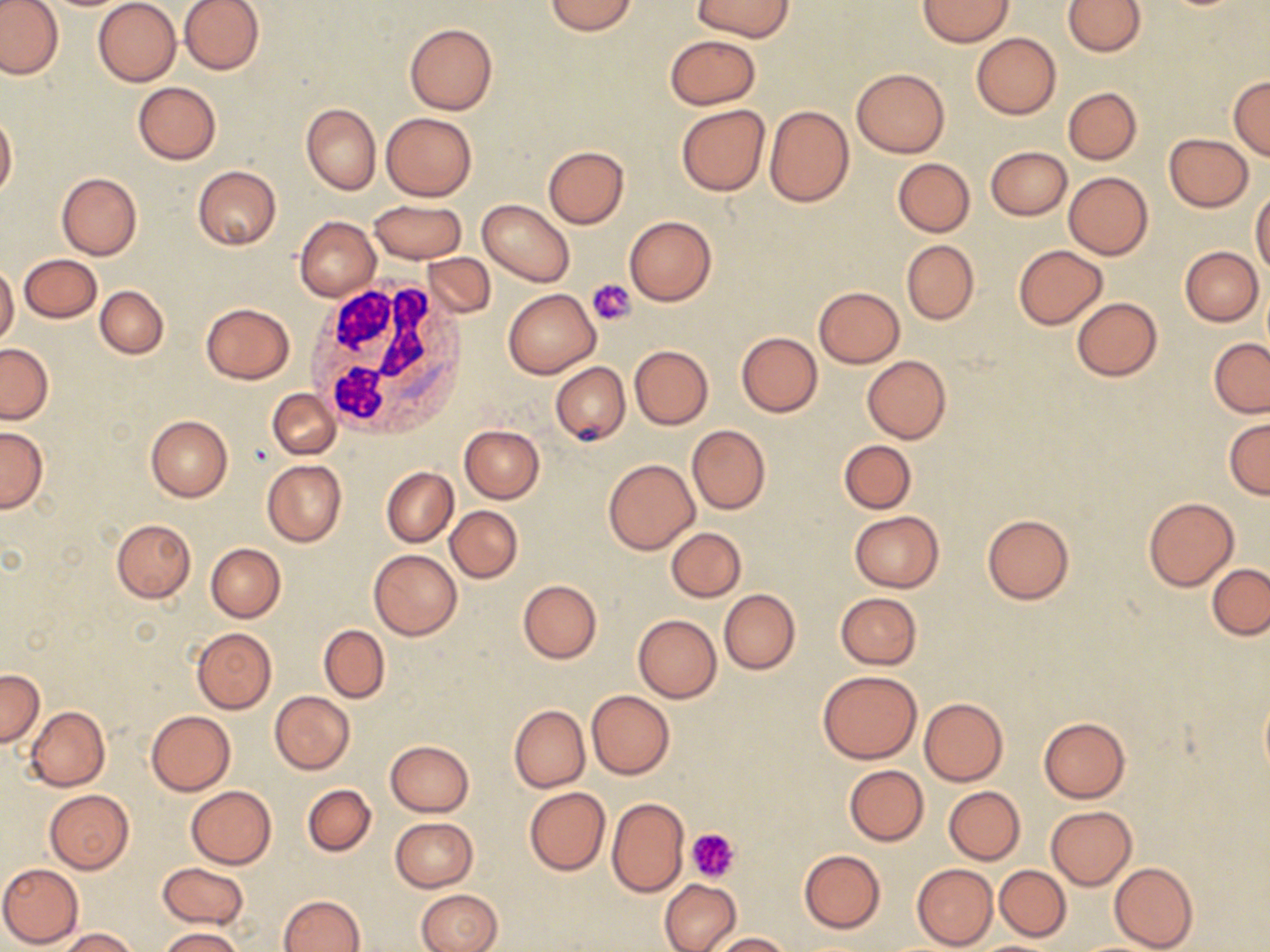
Approximate bounding boxes as (x1,y1)-(x2,y2) corner pairs in pixels. White blood cell locations: (304,275)-(470,439). Uninfected red blood cell locations: (0,0)-(65,80), (93,0)-(181,86), (179,0)-(264,74), (692,0)-(796,40), (918,0)-(1014,47), (1063,0)-(1146,56), (543,1)-(638,35), (404,23)-(497,115), (972,33)-(1061,118), (665,35)-(760,110), (851,68)-(950,158), (1228,77)-(1270,159), (133,82)-(221,164), (1062,87)-(1142,164), (301,103)-(381,193), (676,105)-(769,196), (764,105)-(854,207), (1,111)-(17,200), (381,112)-(477,200), (1164,133)-(1253,211), (543,145)-(629,229), (984,147)-(1072,220), (892,158)-(975,237), (193,165)-(282,249), (1063,172)-(1153,260), (57,173)-(142,259), (1251,191)-(1270,279), (369,199)-(467,263), (477,200)-(575,286), (624,214)-(717,307), (295,215)-(380,301), (901,240)-(979,324), (1014,244)-(1106,328), (1181,246)-(1264,325), (421,252)-(496,318), (19,254)-(102,323), (0,263)-(19,345), (96,285)-(169,358), (814,286)-(905,369), (502,289)-(600,378), (1071,297)-(1163,381), (200,302)-(296,384), (736,332)-(823,417), (1209,339)-(1270,416), (1,344)-(53,423), (629,345)-(712,428), (862,355)-(951,443), (551,362)-(629,444), (268,389)-(339,460), (145,415)-(232,501), (1224,416)-(1270,499), (458,425)-(544,502), (687,425)-(769,515), (0,426)-(48,512), (838,440)-(916,513), (603,459)-(699,554), (263,460)-(347,547), (382,467)-(457,546), (1143,496)-(1239,591), (446,506)-(522,583), (849,511)-(943,591), (981,514)-(1075,605), (111,519)-(196,603), (666,527)-(746,602), (205,543)-(286,621), (369,549)-(462,640), (1208,563)-(1270,639), (518,579)-(601,663), (719,589)-(799,674), (834,592)-(921,669), (633,614)-(722,702), (319,625)-(390,702), (192,628)-(277,713), (0,668)-(43,746), (817,671)-(922,764), (1259,687)-(1270,784), (586,690)-(675,778), (270,691)-(355,775), (919,697)-(1008,786), (509,705)-(589,792), (26,706)-(110,790), (146,711)-(235,795), (1039,716)-(1130,802), (385,740)-(473,816), (844,764)-(929,846), (302,784)-(376,856), (943,785)-(1026,864), (186,786)-(277,868), (524,786)-(611,876), (45,789)-(134,873), (606,797)-(688,896), (1046,806)-(1136,890), (391,817)-(477,891), (799,849)-(885,932), (0,862)-(83,949), (1108,862)-(1198,952), (157,863)-(248,928), (911,864)-(998,949), (995,865)-(1070,941), (660,879)-(741,952), (417,889)-(503,952), (278,894)-(364,952), (58,928)-(138,951), (159,928)-(242,952), (711,932)-(791,951). Platelet locations: (588,278)-(636,325), (688,827)-(739,881). Slide-level diagnosis: negative for blood parasites. One field of a larger specimen. 1000x magnification. Light microscopy. Image is 1270×952 pixels. May-Grünwald-Giemsa stain. Thin blood smear.